Point out each Plasmodium parasite.
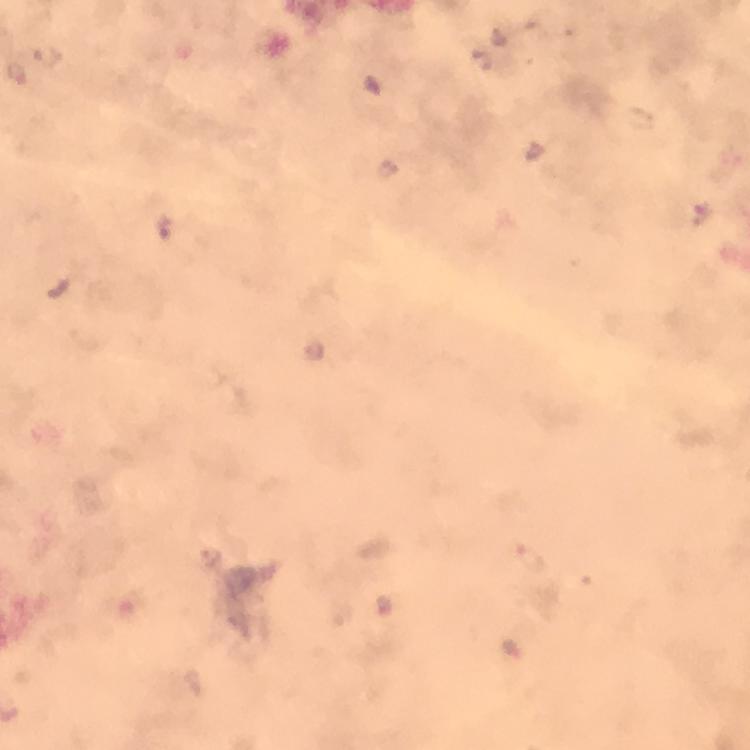

Approximate object centers, in pixels from the top-left corner.
Plasmodium parasites: (x=698, y=216), (x=533, y=560).

preparation = thick smear
magnification = 100x
image size = 750×750 pixels
capture = smartphone mounted on the microscope
stain = Giemsa
context = from a malaria diagnostic workup
immersion oil = used
cropped from = one field of view